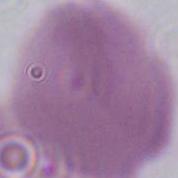
{
  "identification": "erythrocyte",
  "modality": "micrograph",
  "magnification": "1000x"
}